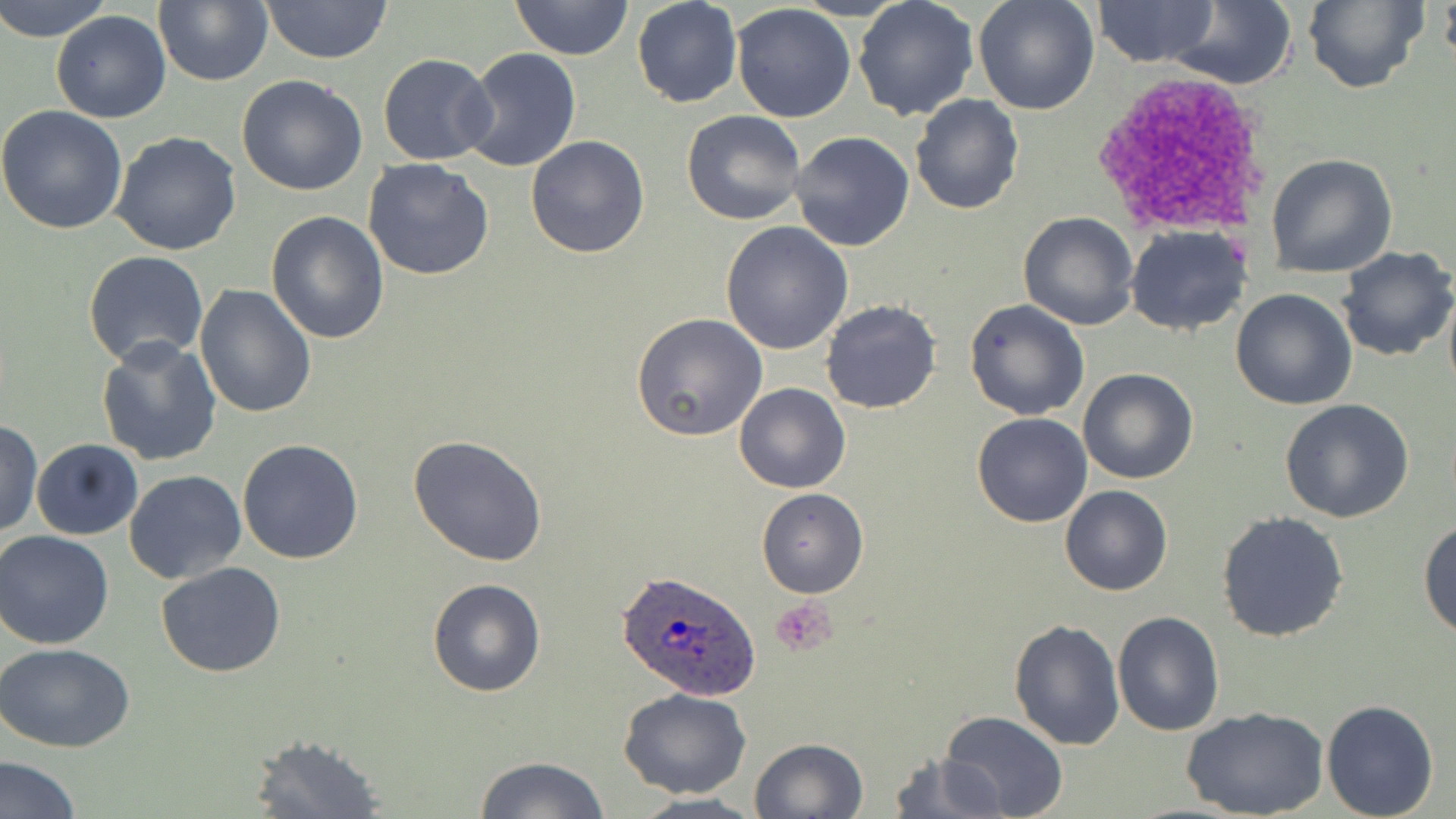

Summary:
  - Coordinate format: approximate bounding boxes as (x1,y1)-(x2,y2) corner pairs in pixels
  - Plasmodium ovale-infected red blood cell locations: (619,571)-(764,699)
  - Platelet locations: (772,597)-(837,655)
  - Uninfected red blood cell locations: (0,0)-(114,43), (153,0)-(272,88), (259,0)-(393,64), (510,0)-(633,61), (972,0)-(1100,115), (1164,0)-(1298,90), (1301,0)-(1427,92), (1440,0)-(1456,70), (631,1)-(741,108), (853,1)-(979,120), (1094,1)-(1218,67), (732,3)-(856,121), (51,9)-(171,123), (459,49)-(581,173), (377,53)-(497,166), (237,74)-(367,195), (909,94)-(1024,215), (0,105)-(129,233), (681,110)-(807,226), (110,131)-(241,256), (789,131)-(915,251), (525,135)-(651,258), (1267,152)-(1398,277), (362,158)-(495,281), (265,210)-(390,343), (1018,211)-(1141,329), (722,220)-(853,355), (1125,226)-(1251,335), (1335,246)-(1456,362), (82,251)-(209,369), (194,285)-(316,418), (1443,286)-(1456,406), (1231,288)-(1358,409), (821,300)-(942,414), (964,300)-(1089,421), (630,313)-(769,443), (95,336)-(221,466), (1078,367)-(1197,484), (734,382)-(850,494), (1280,399)-(1414,522), (972,413)-(1093,527), (1,418)-(43,537), (407,434)-(550,565), (33,439)-(142,540), (237,439)-(364,565), (124,470)-(247,586), (1060,486)-(1172,596), (756,488)-(868,597), (1216,512)-(1349,644), (1418,518)-(1456,639), (0,530)-(114,649), (156,562)-(287,678), (428,577)-(545,697), (1113,610)-(1225,736), (1008,620)-(1125,751), (1,643)-(134,751), (618,687)-(751,798), (1320,699)-(1439,819), (1182,708)-(1327,819), (939,710)-(1071,819), (247,734)-(386,818), (750,737)-(871,819), (885,751)-(1006,819), (0,754)-(81,819), (473,756)-(610,819), (629,792)-(767,819)
  - Slide-level diagnosis: Plasmodium ovale
  - Field of view: one of a larger specimen
  - Image size: 1456×819 pixels
  - Preparation: thin blood film
  - Magnification: 1000x
  - Modality: light microscopy
  - Stain: May-Grünwald-Giemsa